Describe the morphology of the red blood cells.
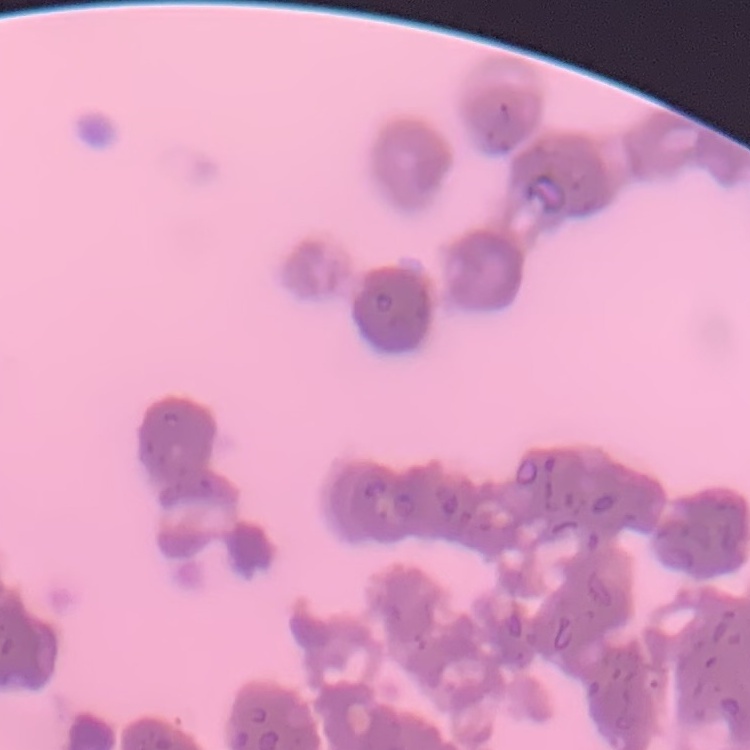

They show rouleaux formation.

Summary:
  - Image type: square crop of a larger photomicrograph
  - Preparation: thin blood smear
  - Stain: Field's or Giemsa